Locate every uninfected red blood cell.
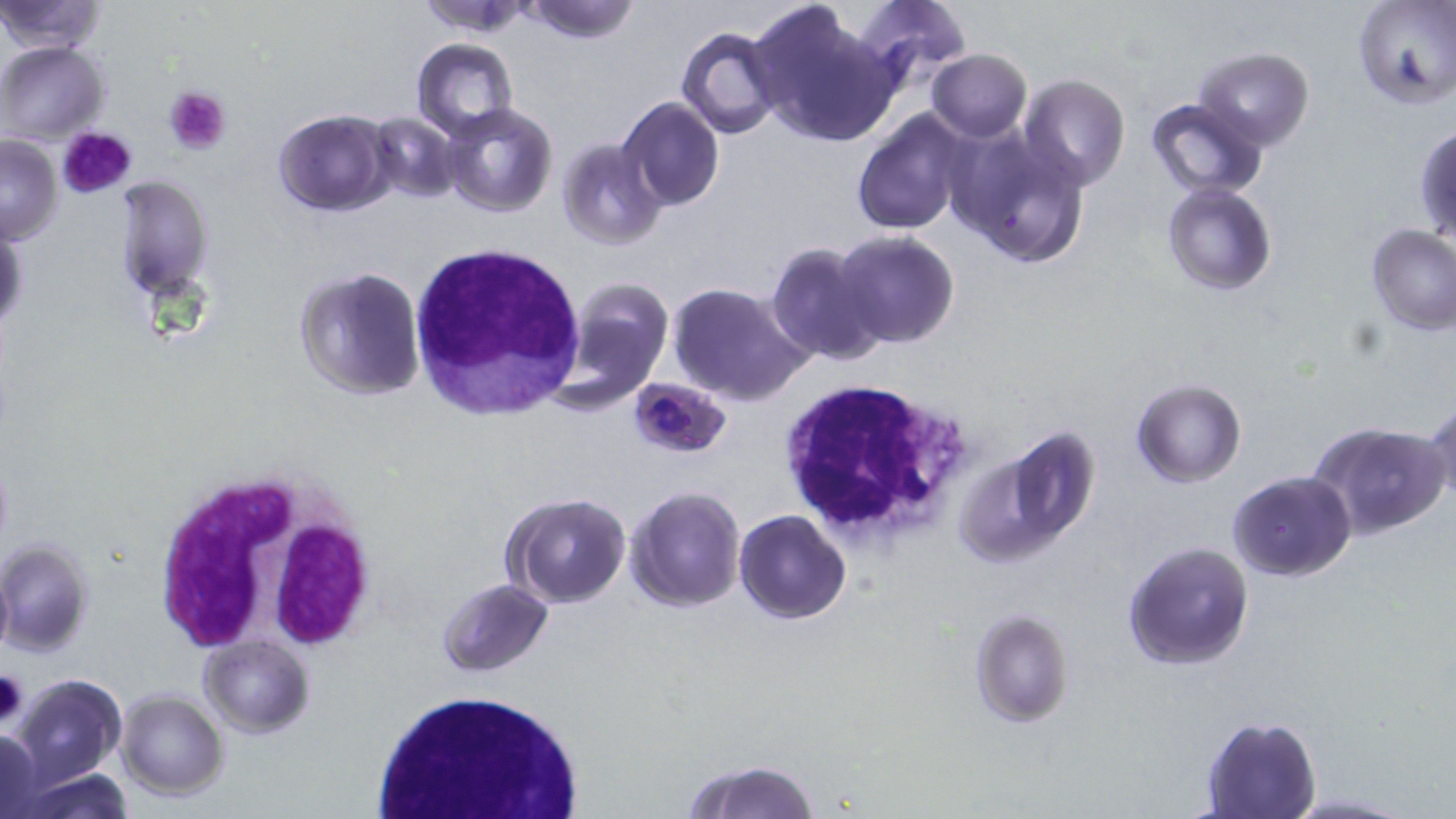

Approximate bounding boxes as (x1, y1, x2, y2) in pixels.
Uninfected red blood cells: (0, 0, 105, 54), (417, 0, 537, 35), (519, 0, 642, 44), (853, 0, 970, 92), (1353, 0, 1456, 110), (746, 2, 894, 149), (676, 26, 784, 138), (411, 38, 518, 138), (1, 41, 110, 142), (1195, 47, 1314, 149), (926, 49, 1032, 142), (1019, 73, 1130, 191), (617, 97, 725, 209), (1146, 97, 1269, 199), (439, 102, 559, 219), (273, 108, 393, 215), (850, 108, 973, 236), (369, 112, 460, 204), (884, 122, 1015, 259), (1415, 123, 1456, 248), (948, 124, 1091, 269), (0, 135, 62, 244), (557, 138, 667, 250), (113, 172, 215, 299), (1162, 181, 1278, 296), (0, 218, 28, 337), (1365, 222, 1456, 336), (833, 231, 959, 348), (766, 242, 885, 365), (292, 266, 426, 400), (561, 277, 676, 405), (667, 282, 807, 404), (1132, 379, 1246, 487), (1425, 400, 1456, 507), (1304, 421, 1449, 539), (955, 425, 1100, 568), (1228, 471, 1355, 582), (626, 485, 746, 613), (503, 493, 631, 608), (734, 510, 852, 624), (0, 539, 94, 657), (1123, 540, 1255, 671), (0, 558, 14, 661), (438, 578, 553, 676), (969, 609, 1074, 727), (200, 635, 314, 737), (11, 674, 126, 787), (116, 689, 229, 800), (1201, 717, 1321, 819), (0, 729, 46, 815), (687, 759, 820, 818), (23, 769, 133, 818).

Summary:
  - Platelet locations: (163, 86, 233, 156), (55, 125, 139, 202), (1, 672, 29, 727)
  - White blood cell locations: (411, 245, 583, 414), (773, 377, 972, 547), (150, 470, 375, 656), (368, 687, 584, 819)
  - Plasmodium falciparum-infected red blood cell locations: (628, 377, 730, 458)
  - Slide-level diagnosis: Plasmodium falciparum
  - Preparation: thin blood film
  - Stain: May-Grünwald-Giemsa
  - Field of view: single
  - Image size: 1456×819 pixels
  - Magnification: 1000x
  - Modality: light microscopy